Point out every malaria parasite and every leukocyte.
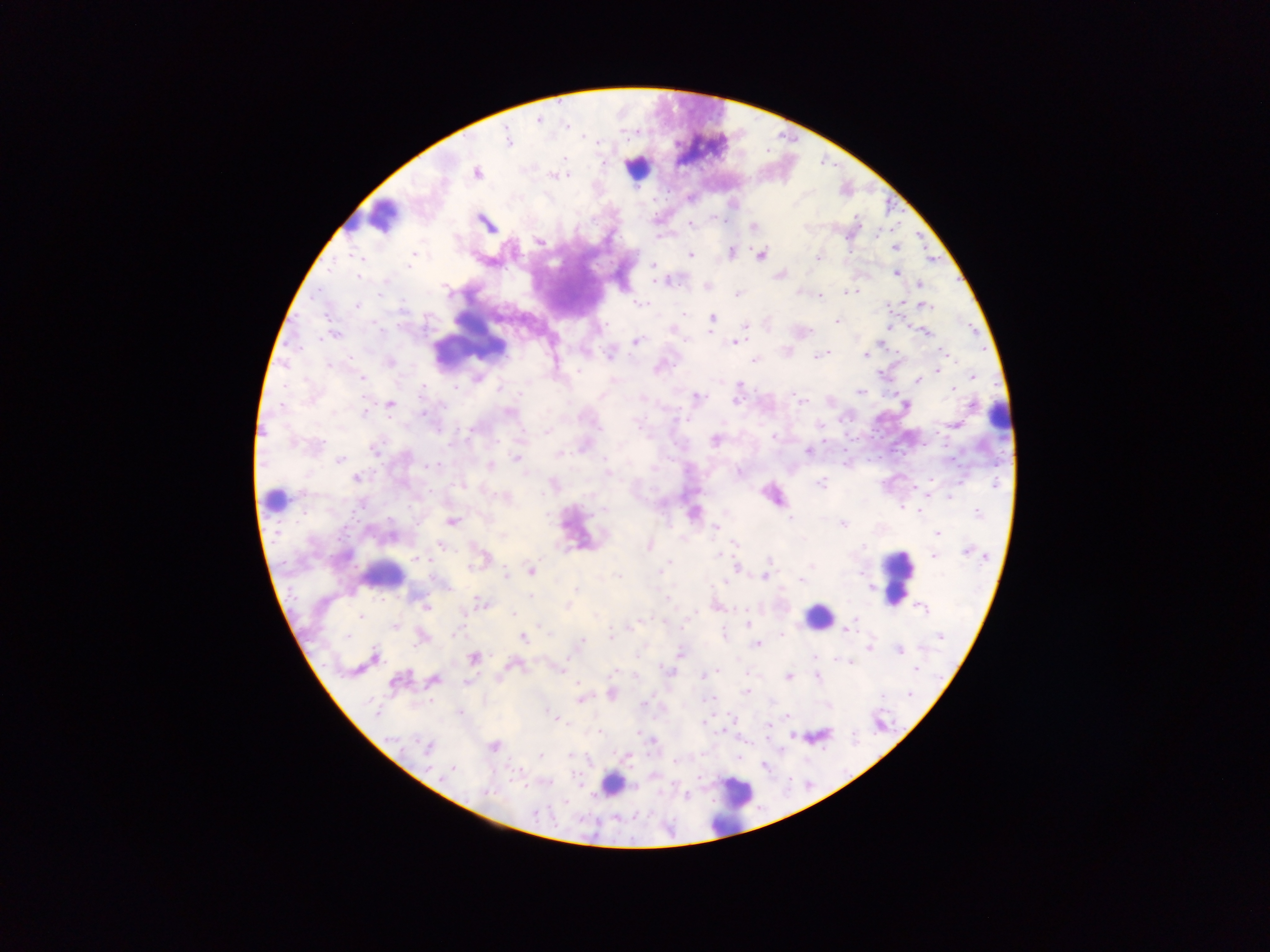

Approximate centers as [x, y] in pixels.
Malaria parasites: [537, 120], [784, 137], [506, 140], [628, 141], [768, 151], [822, 163], [836, 165], [475, 172], [667, 195], [856, 218], [899, 222], [487, 226], [692, 226], [752, 227], [891, 231], [918, 233], [878, 236], [846, 239], [539, 243], [925, 246], [896, 248], [732, 252], [849, 252], [759, 255], [355, 256], [691, 256], [361, 257], [818, 257], [409, 262], [406, 266], [652, 267], [329, 271], [360, 275], [896, 275], [385, 280], [658, 282], [918, 283], [705, 286], [447, 290], [858, 291], [737, 294], [821, 298], [402, 303], [638, 303], [888, 304], [356, 306], [927, 306], [712, 314], [686, 315], [838, 321], [710, 323], [970, 324], [744, 326], [891, 328], [671, 330], [924, 333], [334, 334], [685, 338], [636, 342], [733, 344], [297, 346], [896, 351], [945, 352], [610, 353], [826, 353], [951, 353], [866, 355], [812, 357], [477, 358], [753, 360], [557, 361], [328, 364], [939, 371], [476, 374], [973, 375], [360, 376], [917, 382], [738, 384], [456, 387], [500, 388], [953, 388], [423, 391], [860, 393], [696, 396], [800, 399], [283, 403], [906, 404], [971, 405], [422, 412], [510, 412], [365, 414], [682, 417], [636, 421], [956, 423], [819, 426], [876, 429], [469, 431], [545, 432], [774, 437], [858, 439], [295, 443], [317, 443], [925, 443], [375, 449], [581, 449], [808, 449], [558, 453], [605, 457], [881, 457], [516, 458], [954, 459], [340, 460], [437, 464], [432, 465], [489, 466], [608, 472], [357, 479], [931, 481], [552, 483], [821, 483], [463, 487], [914, 488], [948, 496], [604, 508], [903, 508], [977, 513], [920, 515], [790, 519], [359, 520], [451, 521], [297, 524], [844, 524], [715, 528], [502, 536], [937, 536], [339, 539], [735, 544], [440, 546], [649, 546], [965, 552], [933, 556], [416, 558], [771, 560], [666, 563], [736, 566], [811, 566], [531, 572], [617, 575], [505, 576], [765, 577], [802, 583], [723, 584], [576, 589], [417, 597], [527, 597], [480, 601], [422, 603], [566, 606], [924, 609], [512, 614], [361, 616], [663, 621], [633, 624], [747, 625], [396, 627], [454, 632], [846, 632], [610, 636], [725, 636], [782, 636], [942, 637], [348, 638], [522, 638], [583, 638], [756, 645], [870, 645], [899, 651], [375, 654], [812, 657], [474, 658], [851, 662], [508, 663], [613, 670], [914, 670], [669, 671], [718, 671], [700, 676], [495, 678], [788, 678], [817, 679], [434, 680], [395, 682], [465, 682], [575, 682], [611, 693], [745, 693], [430, 701], [644, 701], [581, 702], [373, 706], [557, 719], [560, 720], [701, 722], [596, 731], [599, 734], [791, 736], [653, 743], [425, 749], [570, 757], [629, 757], [540, 758], [737, 759], [451, 769], [699, 778], [488, 792], [536, 813].
Leukocytes: [635, 169], [387, 215], [353, 219], [471, 337], [998, 420], [278, 496], [380, 577], [896, 578], [822, 614], [612, 785], [728, 807].

Image is 1270×952 pixels. Sample from Ghana. Thick blood smear. Mobile-phone photograph taken through the microscope. Single field of view.